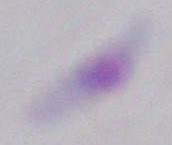

identification = Toxoplasma gondii
modality = photomicrograph
magnification = 1000x